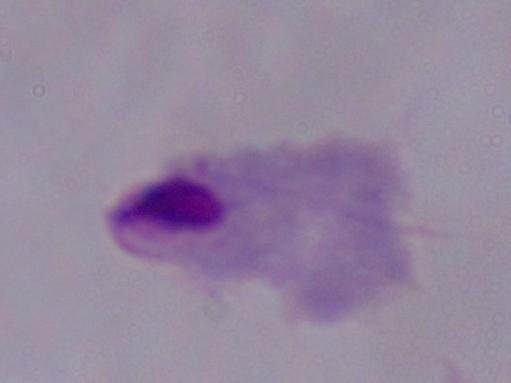 Photomicrograph. 1000x magnification. A trichomonad is seen.